Name the blood parasite species.
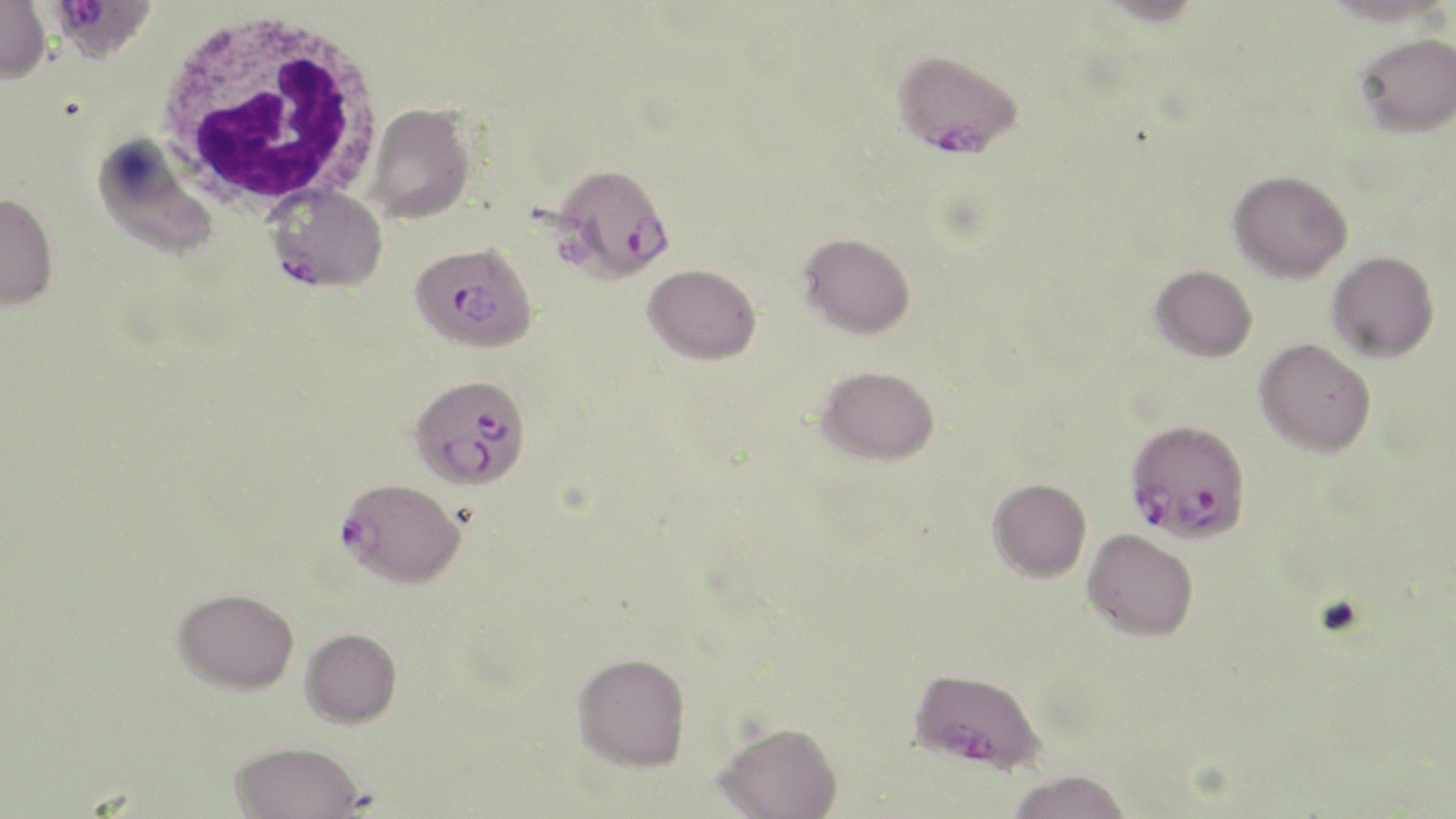

Plasmodium falciparum.

stain = May-Grünwald-Giemsa
field of view = one of a larger specimen
modality = optical microscopy
Plasmodium falciparum-infected red blood cell locations (subset) = approximate bounding boxes as [x1, y1, x2, y2] in pixels: [47, 0, 157, 64], [891, 48, 1022, 158], [268, 184, 388, 292], [409, 241, 538, 353], [409, 373, 530, 490], [1125, 418, 1252, 544], [337, 477, 466, 588], [909, 667, 1046, 773]
preparation = thin blood film
magnification = 1000x
image size = 1456×819 pixels
uninfected red blood cell locations (subset) = approximate bounding boxes as [x1, y1, x2, y2] in pixels: [0, 1, 51, 84], [1327, 1, 1453, 26], [1355, 32, 1456, 138], [366, 102, 475, 224], [93, 133, 219, 260], [1228, 170, 1352, 283], [0, 192, 58, 310], [798, 231, 916, 339], [1327, 251, 1440, 363], [643, 263, 761, 364], [1151, 265, 1258, 362], [1254, 338, 1376, 457], [816, 365, 941, 465], [988, 477, 1091, 581], [1082, 529, 1199, 641], [173, 587, 299, 693], [300, 627, 402, 726], [572, 652, 691, 771], [715, 721, 843, 819], [230, 740, 364, 819], [1005, 769, 1131, 819]
white blood cell locations = approximate bounding boxes as [x1, y1, x2, y2] in pixels: [153, 10, 385, 212]